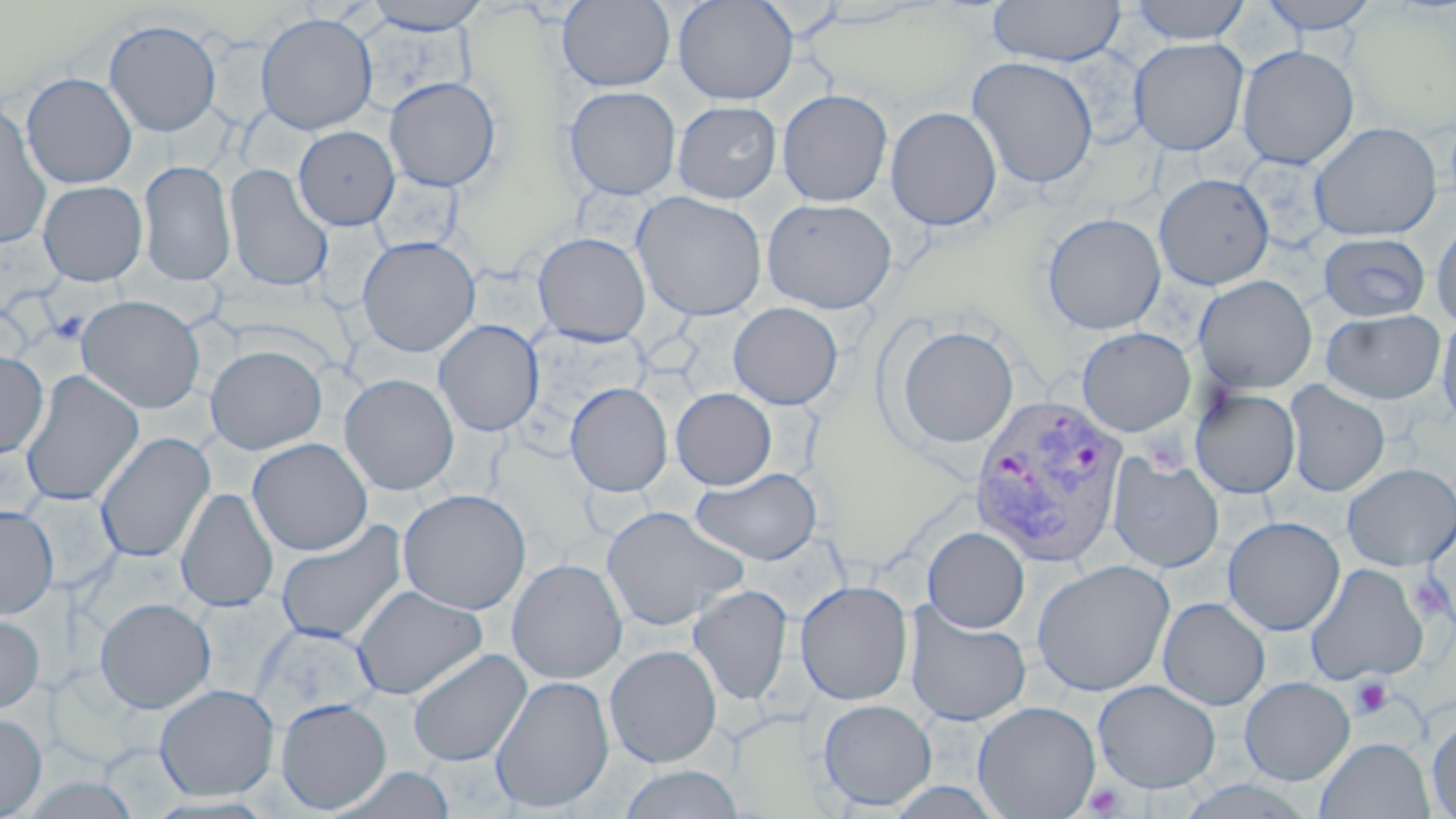

Summary:
  - Coordinate format: approximate bounding boxes as (x1, y1, x2, y2) in pixels
  - Uninfected red blood cell locations: (362, 0, 493, 34), (672, 0, 798, 105), (988, 0, 1125, 67), (1129, 0, 1251, 44), (1258, 0, 1382, 34), (558, 1, 675, 91), (255, 12, 378, 135), (103, 19, 222, 137), (1129, 37, 1249, 156), (1236, 45, 1359, 169), (966, 56, 1099, 189), (21, 72, 137, 189), (384, 76, 501, 191), (564, 86, 682, 199), (776, 88, 893, 207), (673, 100, 781, 203), (0, 102, 52, 248), (885, 107, 1002, 230), (1309, 122, 1442, 241), (293, 126, 400, 230), (137, 160, 236, 286), (224, 163, 334, 292), (1154, 173, 1275, 290), (38, 180, 148, 286), (631, 191, 767, 321), (762, 197, 896, 314), (1042, 212, 1166, 334), (1431, 217, 1456, 330), (533, 232, 651, 345), (1318, 232, 1432, 321), (357, 235, 480, 357), (1193, 275, 1318, 394), (76, 295, 205, 413), (728, 302, 843, 410), (1321, 309, 1446, 404), (1436, 313, 1456, 431), (433, 319, 544, 437), (895, 324, 1019, 448), (1076, 327, 1196, 437), (205, 345, 327, 454), (0, 350, 48, 459), (20, 370, 144, 507), (339, 373, 459, 495), (1284, 380, 1390, 498), (565, 382, 672, 497), (671, 388, 777, 490), (1189, 388, 1300, 499), (95, 432, 215, 564), (247, 437, 372, 556), (1107, 454, 1225, 573), (1342, 462, 1456, 571), (691, 467, 822, 565), (176, 487, 278, 613), (398, 488, 531, 615), (0, 504, 59, 619), (601, 505, 747, 631), (1222, 516, 1345, 636), (276, 520, 407, 644), (923, 526, 1030, 632), (506, 558, 628, 684), (1032, 559, 1175, 696), (1304, 562, 1431, 685), (795, 579, 913, 705), (688, 584, 793, 705), (352, 585, 487, 700), (95, 597, 216, 713), (1158, 597, 1270, 711), (905, 605, 1031, 726), (0, 611, 45, 713), (604, 643, 722, 767), (407, 648, 531, 767), (490, 674, 614, 812), (1239, 676, 1355, 784), (1093, 679, 1220, 793), (154, 684, 279, 800), (276, 698, 392, 813), (817, 698, 937, 810), (973, 700, 1101, 818), (0, 713, 47, 818), (1426, 714, 1456, 817), (1316, 736, 1434, 819), (618, 765, 745, 819), (331, 766, 456, 819), (14, 774, 144, 818)
  - Platelet locations: (1409, 574, 1453, 623), (1350, 677, 1393, 719), (1083, 783, 1125, 817)
  - Plasmodium vivax-infected red blood cell locations: (967, 393, 1129, 566)
  - Slide-level diagnosis: Plasmodium vivax
  - Field of view: single
  - Preparation: thin blood smear
  - Magnification: 1000x
  - Stain: May-Grünwald-Giemsa
  - Modality: optical microscopy
  - Image size: 1456×819 pixels